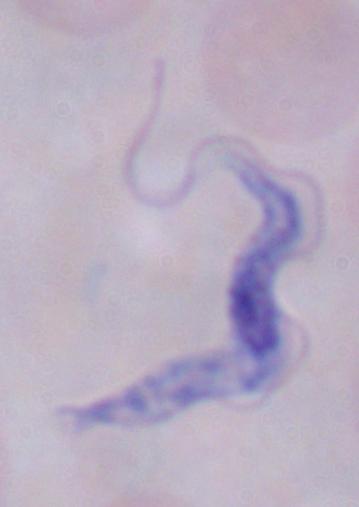

{
  "magnification": "1000x",
  "modality": "photomicrograph",
  "identification": "trypanosome"
}